Identify the cell.
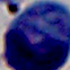

This is a leukocyte.

Captured at 1000x magnification. Micrograph.